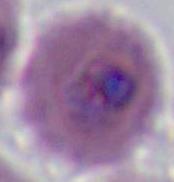

modality = micrograph
identification = Plasmodium
magnification = 400x or 1000x